Assess this cell for malaria.
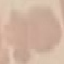
Uninfected.

Giemsa stain. Thin blood smear. Photographed with a smartphone camera at the microscope eyepiece. Automatically extracted cell patch, resized to 64 × 64 pixels.